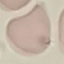 Malaria status: uninfected. Thin smear of blood. Photographed with a smartphone camera at the microscope eyepiece. Giemsa-stained preparation. Automatically extracted cell patch, resized to 64 × 64 pixels.